Give a bounding box for every leukocyte visible.
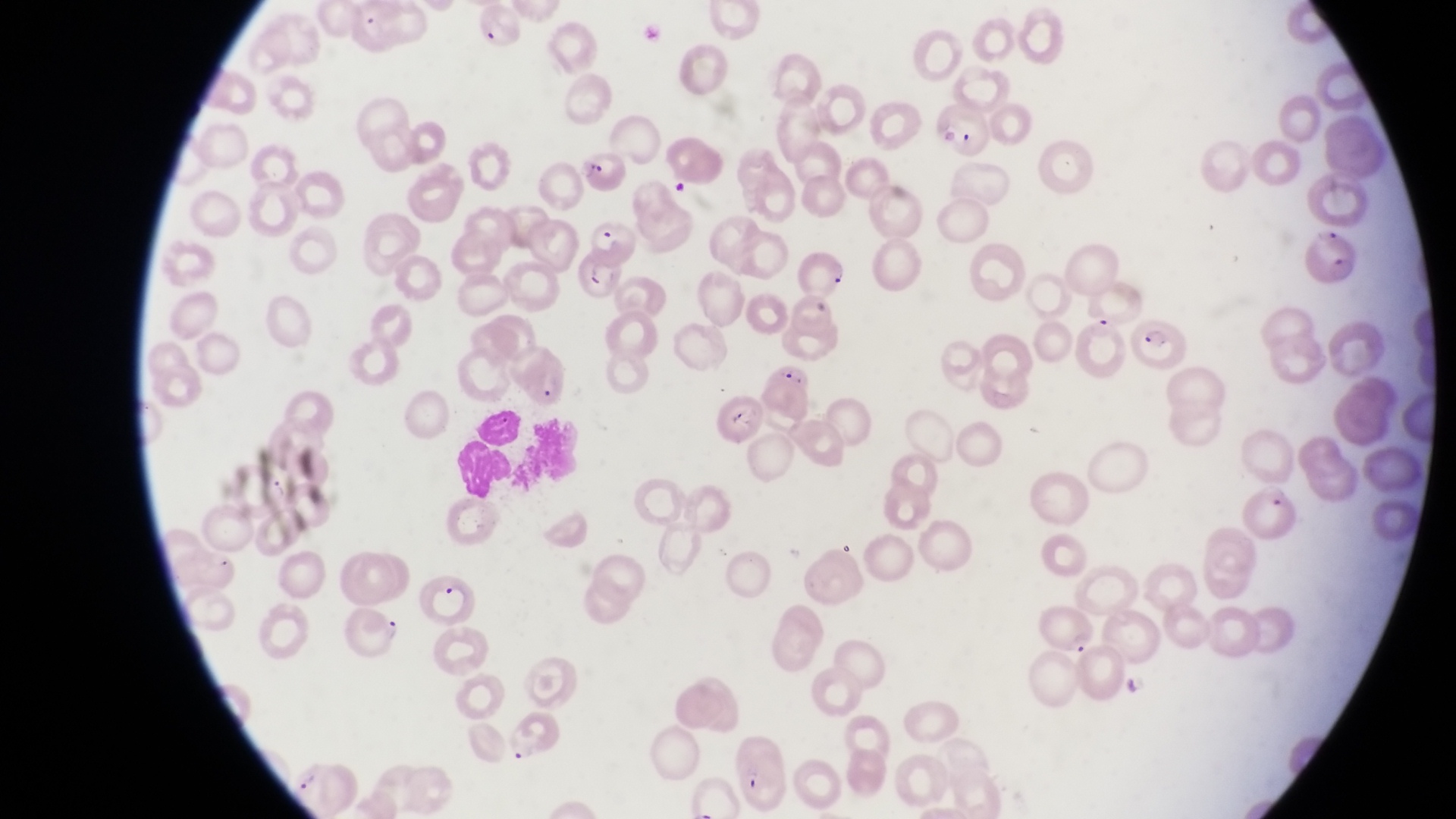
Approximate bounding boxes as (left, top, right, bottom) in pixels.
Leukocytes: (473, 400, 522, 449), (455, 444, 514, 500).

country = Uganda
parasitised red blood cell locations = approximate bounding boxes as (left, top, right, bottom) in pixels: (470, 7, 523, 49), (934, 100, 992, 159), (573, 155, 634, 197), (1307, 224, 1360, 290), (568, 246, 623, 298), (788, 291, 844, 338), (1131, 310, 1190, 371), (510, 346, 574, 413), (713, 389, 771, 444), (1241, 485, 1301, 535), (415, 566, 487, 627), (1034, 601, 1098, 659), (343, 605, 402, 657), (729, 727, 792, 812)
magnification = 1000x
image size = 1456×819 pixels
capture = smartphone photograph through the eyepiece of an Olympus CX-23 microscope
preparation = thin blood smear
field of view = single